Name the parasite shown.
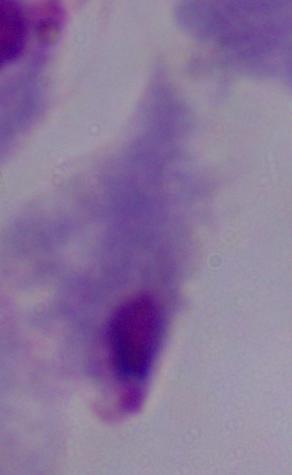
This is a trichomonad.

magnification = 1000x
modality = micrograph